Report the malaria status of this cell.
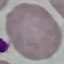

Uninfected.

Thin blood film. Photographed with a smartphone camera at the microscope eyepiece. Cell patch, automatically extracted from a larger field of view and resized to 64 × 64 pixels. Giemsa stain.